Comment on the morphology of the erythrocytes.
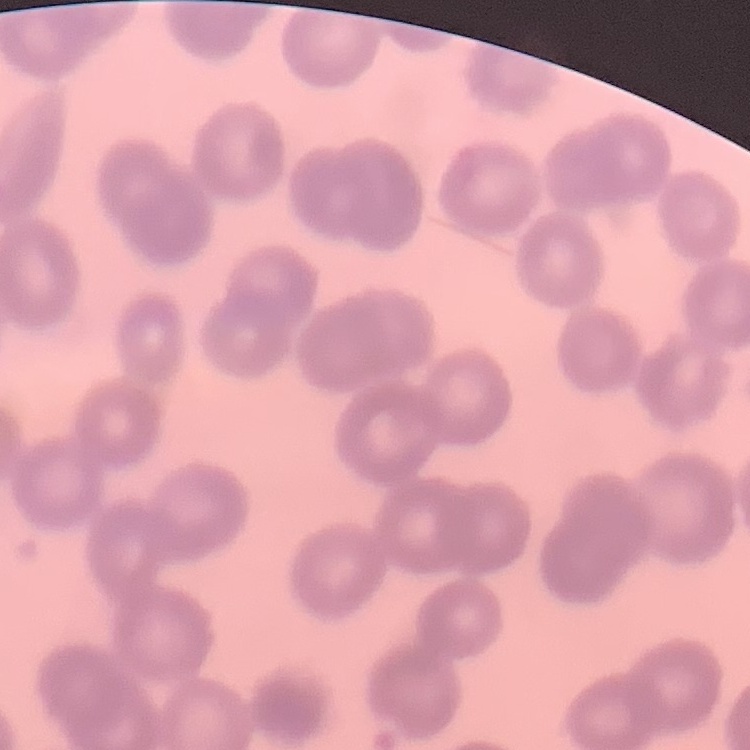
No rouleaux formation.

Square crop of a larger photomicrograph. Stained with either Field's or Giemsa. Thin blood smear.